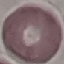
Result: no malaria parasites seen. Automatically extracted cell patch, resized to 64 × 64 pixels. Thin smear of blood. Photographed with a smartphone camera at the microscope eyepiece. Giemsa stain.